Point out each Plasmodium parasite.
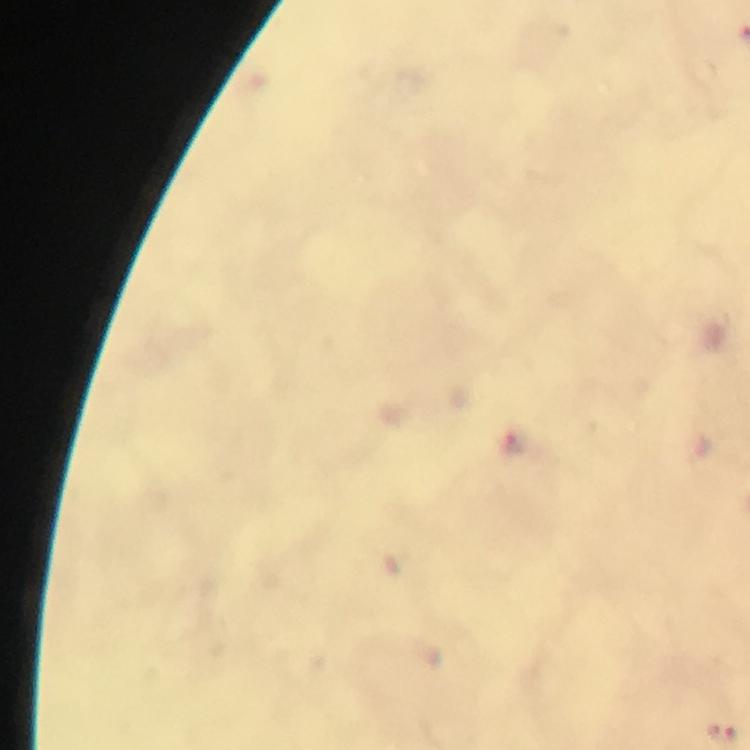

Approximate centers as {x, y} in pixels.
Plasmodium parasites: {517, 446}.

Summary:
  - Magnification: 100x
  - Preparation: thick blood smear
  - Cropped from: a single field of view
  - Image size: 750×750 pixels
  - Capture: smartphone camera through the microscope
  - Stain: Giemsa
  - Immersion oil: applied
  - Context: from a malaria diagnostic workup